Report the malaria status of this cell.
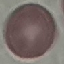
It is uninfected.

Summary:
  - Image type: cell patch, automatically extracted from a larger field of view and resized to 64 × 64 pixels
  - Stain: Giemsa
  - Preparation: thin blood smear
  - Capture: smartphone through the microscope eyepiece